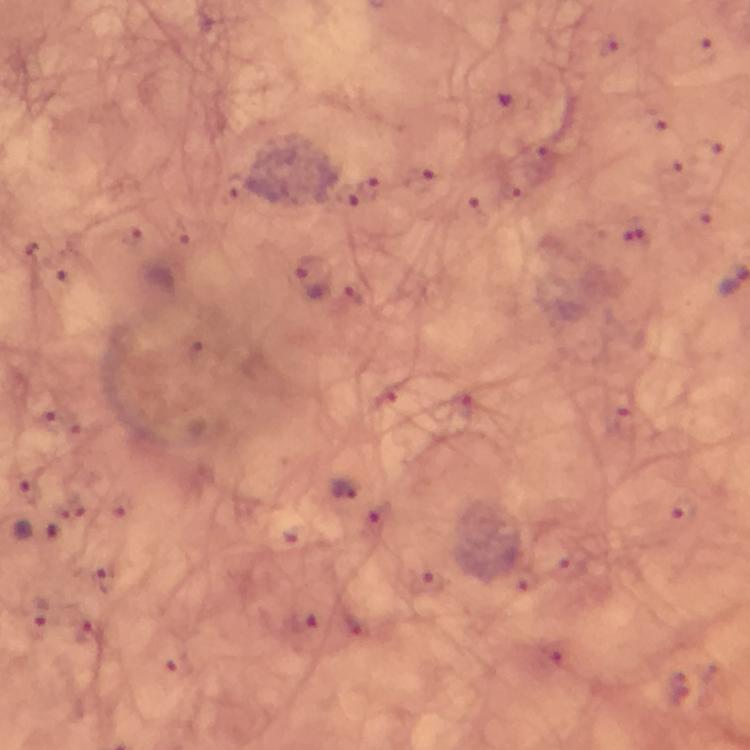

context = from a diagnostic examination for malaria
cropped from = a single field of view
image size = 750×750 pixels
preparation = thick smear
stain = Giemsa
immersion oil = applied
capture = smartphone camera through the microscope
magnification = 100x
malaria parasite locations = approximate centers as [x, y] in pixels: [703, 51], [370, 187], [344, 196], [127, 233], [635, 233], [311, 278], [48, 421], [76, 427], [348, 489], [375, 520], [36, 531], [109, 581], [433, 582], [41, 613]